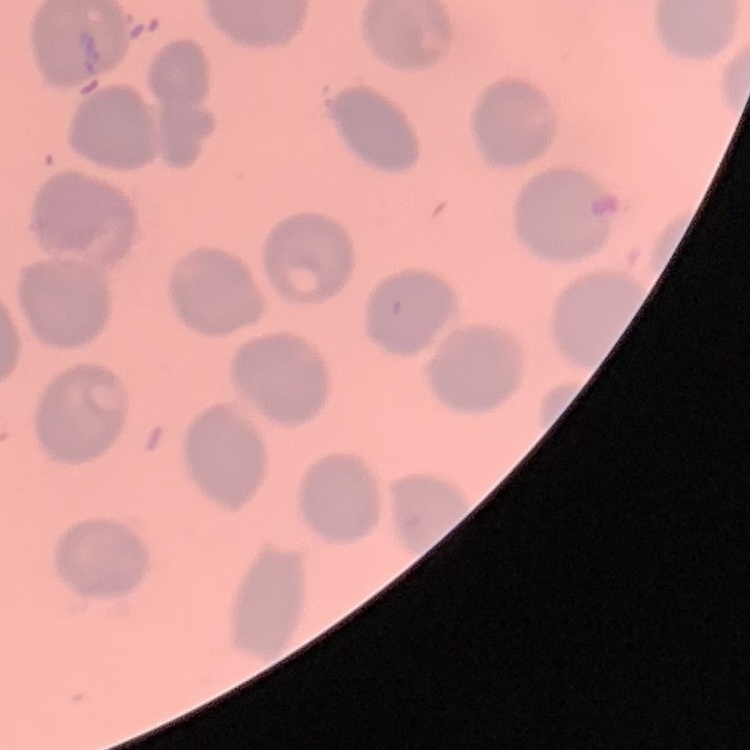

Summary:
  - Erythrocyte morphology: no rouleaux formation
  - Preparation: thin blood smear
  - Image type: square crop of a larger photomicrograph
  - Stain: Field's or Giemsa